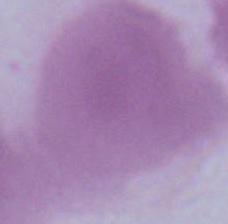

Summary:
  - Magnification: 1000x
  - Identification: red blood cell
  - Modality: photomicrograph